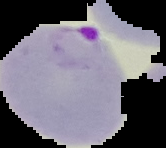
From a thin blood smear. Image is 166×148 pixels. Malaria status: parasitized. The area outside the segmented cell region is set to black.